Describe the morphology of the erythrocytes.
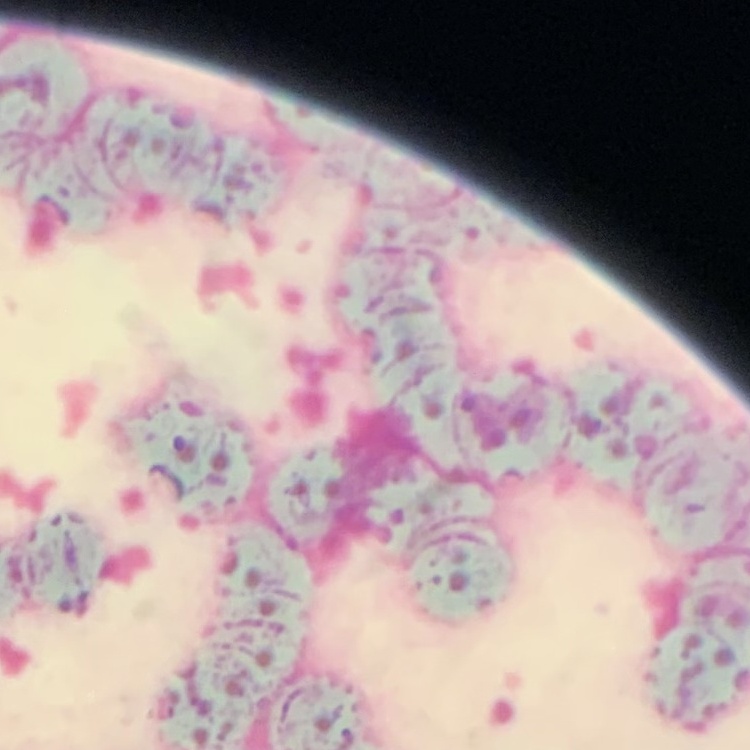

They show rouleaux formation.

Thin blood film. Square crop of a larger photomicrograph. Stained with either Field's or Giemsa.